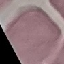
Summary:
  - Result: no malaria parasites seen
  - Preparation: thin blood film
  - Capture: smartphone camera at the microscope eyepiece
  - Stain: Giemsa
  - Image type: cell patch, automatically extracted from a larger field of view and resized to 64 × 64 pixels